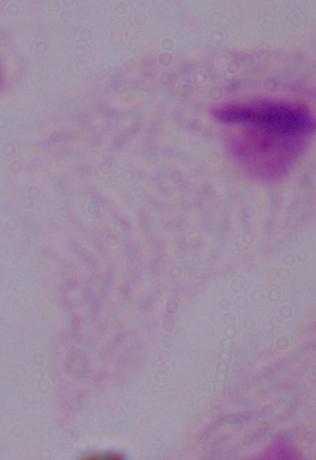

A trichomonad is seen. 1000x magnification. Micrograph.